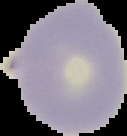

Summary:
  - Result: negative for Plasmodium parasites
  - Image size: 127×136 pixels
  - Preparation: thin blood smear
  - Image type: cell region segmented out of the field of view; surrounding area masked to black